State which parasite is depicted.
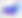
Toxoplasma gondii.

magnification = 400x
modality = photomicrograph